Assess the morphology of the erythrocytes.
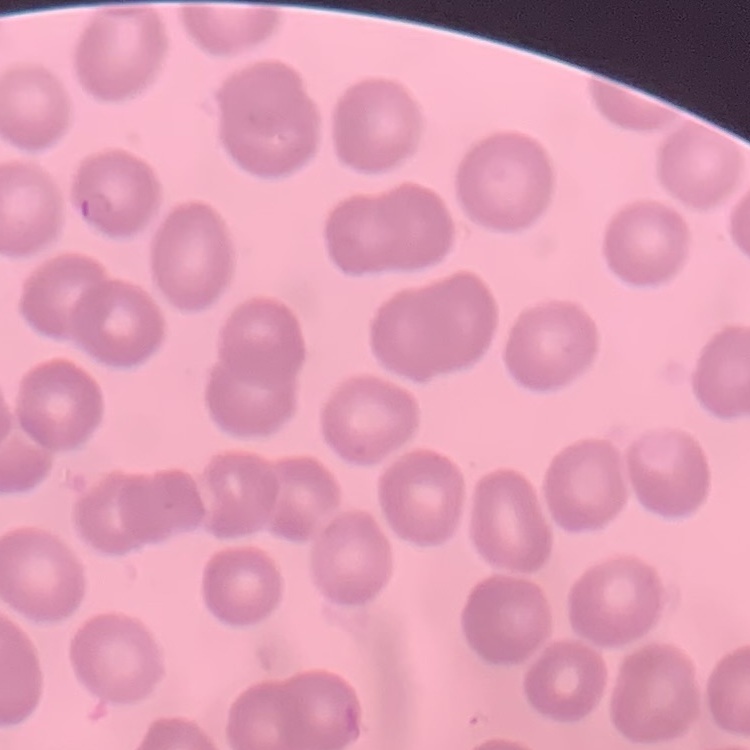

They show no rouleaux formation.

Summary:
  - Image type: square crop of a larger photomicrograph
  - Stain: Field's or Giemsa
  - Preparation: thin peripheral smear